Identify the parasite.
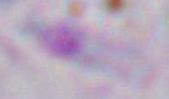
Toxoplasma gondii.

magnification: 1000x
modality: micrograph